Assess this cell for malaria.
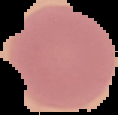

It is uninfected.

preparation = thin blood smear
image size = 118×115 pixels
image type = segmented cell region with the area outside set to black